Outline each uninfected red blood cell.
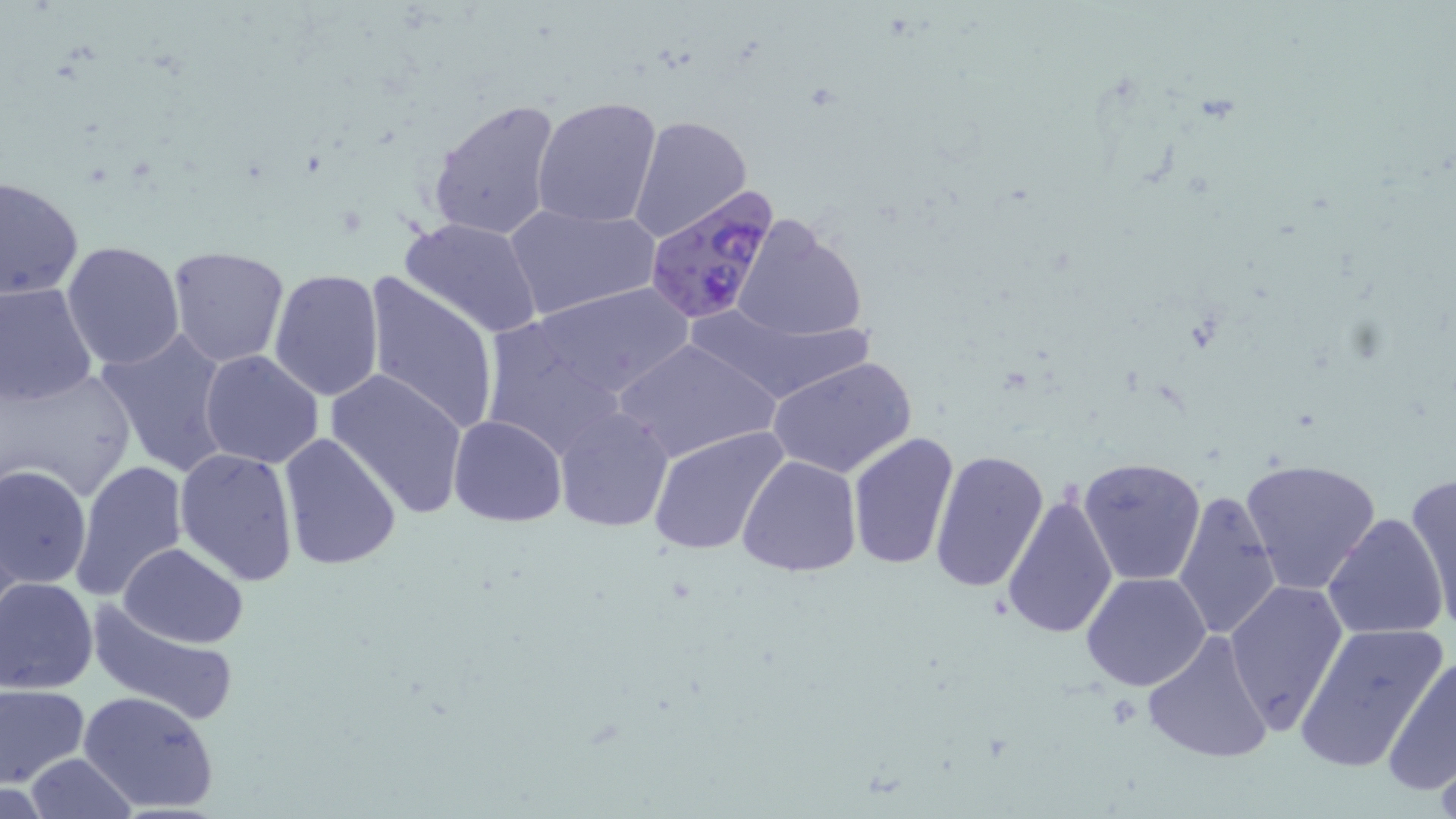
Approximate bounding boxes as (x1, y1, x2, y2) in pixels.
Uninfected red blood cells: (531, 95, 663, 229), (426, 97, 562, 242), (627, 113, 752, 246), (0, 175, 83, 300), (503, 199, 659, 322), (399, 217, 545, 338), (730, 217, 868, 347), (59, 240, 185, 370), (166, 245, 290, 366), (268, 268, 385, 401), (361, 271, 501, 438), (0, 281, 99, 406), (526, 283, 692, 402), (96, 327, 234, 476), (616, 337, 780, 465), (199, 350, 325, 468), (769, 355, 918, 479), (0, 365, 139, 503), (325, 368, 470, 518), (553, 408, 674, 533), (448, 415, 567, 525), (647, 425, 792, 560), (846, 432, 960, 574), (278, 434, 401, 571), (174, 447, 299, 586), (930, 449, 1050, 595), (736, 453, 861, 578), (1077, 456, 1208, 587), (1239, 457, 1385, 597), (71, 459, 190, 602), (1, 465, 91, 592), (1404, 472, 1456, 633), (1002, 488, 1118, 640), (1174, 488, 1281, 640), (1323, 511, 1451, 640), (119, 543, 248, 648), (1082, 570, 1213, 692), (0, 577, 99, 693), (1224, 580, 1347, 733), (87, 600, 241, 726), (1292, 622, 1448, 774), (1141, 629, 1276, 763), (1382, 655, 1456, 796), (0, 684, 87, 787), (79, 691, 220, 815), (23, 754, 137, 819).

Plasmodium falciparum-infected red blood cell locations: (643, 189, 780, 326). Slide-level diagnosis: Plasmodium falciparum. 1000x magnification. May-Grünwald-Giemsa-stained preparation. Thin blood film. Image is 1456×819 pixels. One field of a larger specimen. Light microscopy.